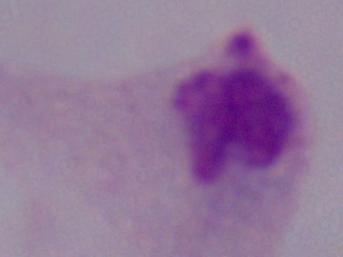
A trichomonad is seen. Micrograph. Captured at 1000x magnification.